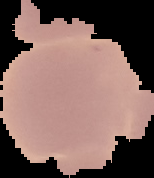

From a thin blood smear. Malaria status: uninfected. Image is 154×178 pixels. Segmented cell region on a black background.